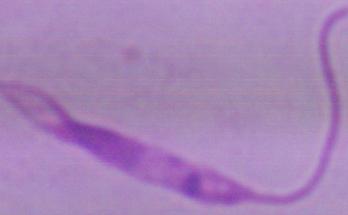
{
  "modality": "micrograph",
  "magnification": "1000x",
  "identification": "Leishmania"
}